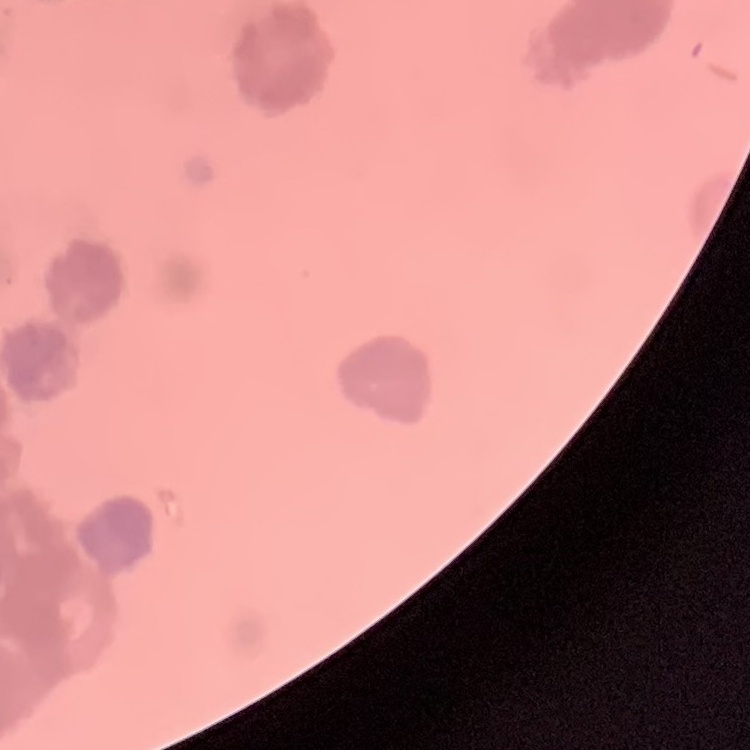

The red blood cells exhibit rouleaux formation. One tile cut from a larger photomicrograph. Stained with either Field's or Giemsa. Thin blood film.